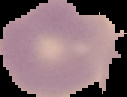

{
  "result": "no Plasmodium parasites detected",
  "image_type": "segmented cell region with the area outside set to black",
  "image_size": "127×97 pixels",
  "preparation": "thin blood film"
}